Comment on the morphology of the erythrocytes.
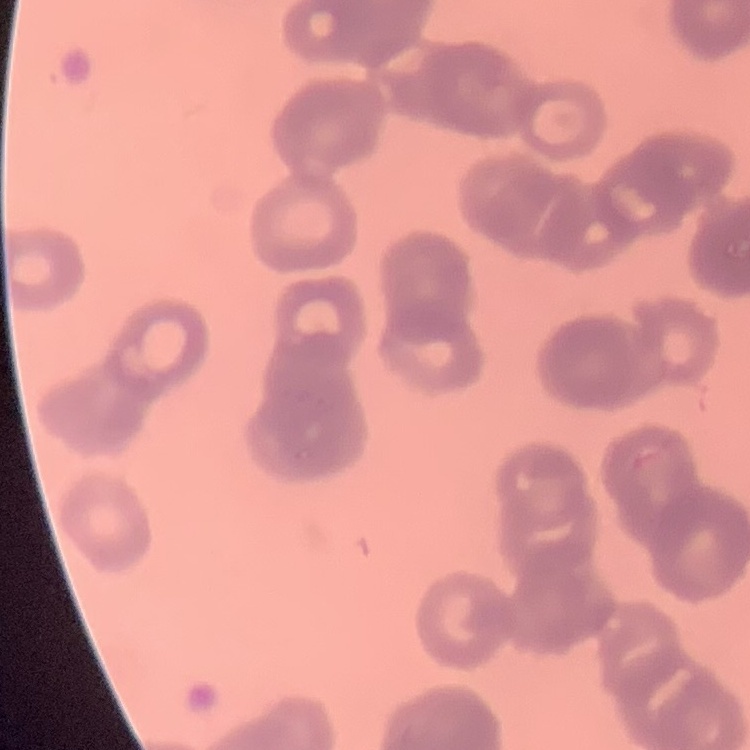

They show rouleaux formation.

Summary:
  - Preparation: thin peripheral smear
  - Stain: Field's or Giemsa
  - Image type: square crop of a larger photomicrograph